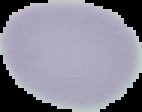
image type = cell region segmented out of the field of view; surrounding area masked to black
result = no malaria parasites seen
image size = 142×112 pixels
preparation = thin blood film